Report the malaria status of this cell.
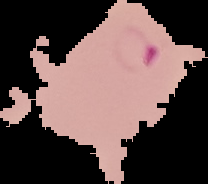
Parasitized.

preparation = thin blood film
image size = 208×184 pixels
image type = segmented cell region with the area outside set to black